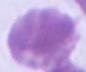

Summary:
  - Magnification: 1000x
  - Identification: red blood cell
  - Modality: micrograph